Identify the cell.
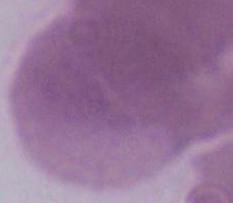

This is an erythrocyte.

Micrograph. Captured at 1000x magnification.